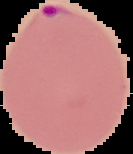

Summary:
  - Image type: cell region segmented out of the field of view; surrounding area masked to black
  - Malaria status: parasitized
  - Preparation: thin blood film
  - Image size: 133×154 pixels